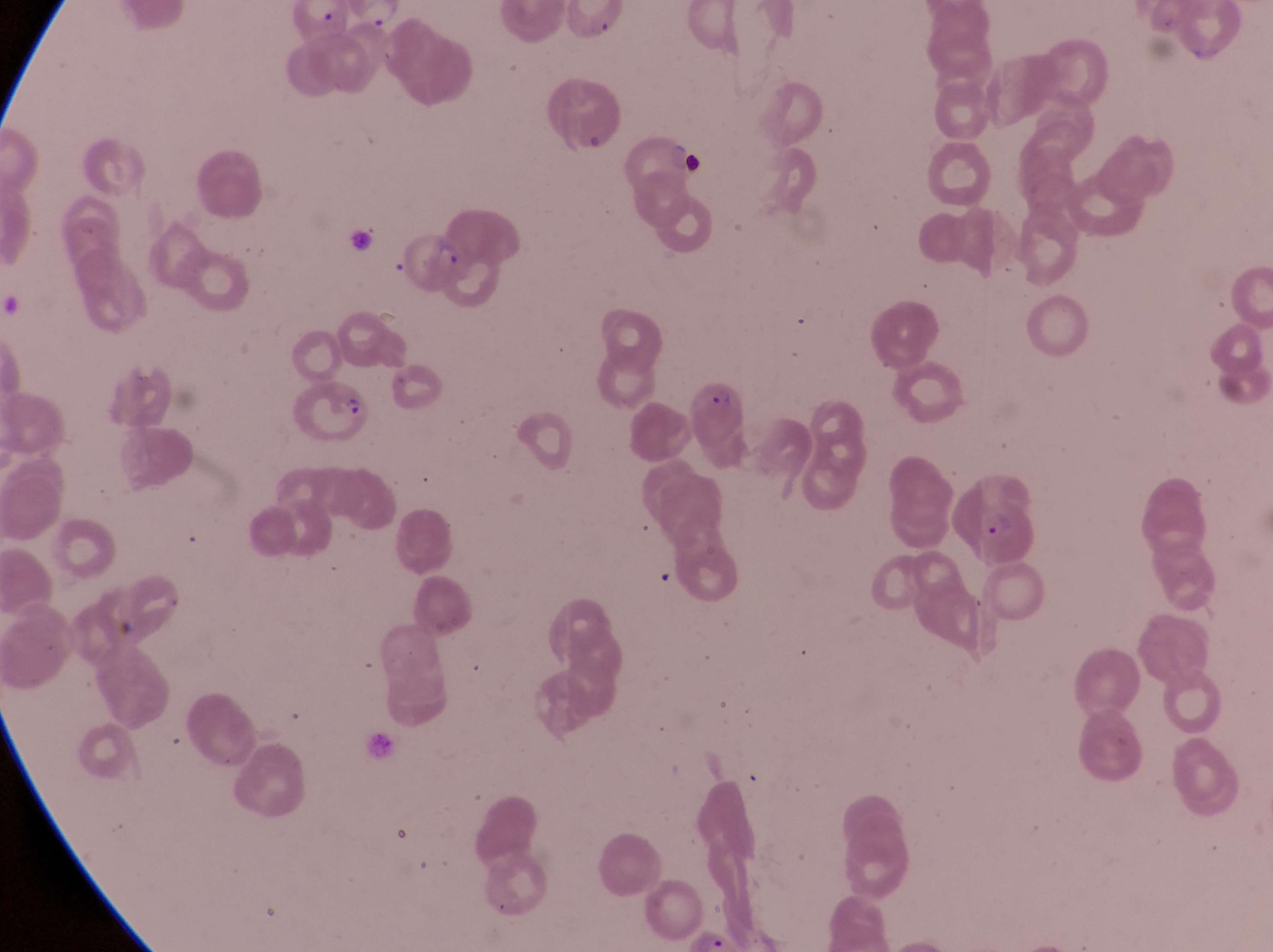
parasitised_red_blood_cell_locations: 'approximate bounding boxes as (left, top, right, bottom) in pixels: (404, 227, 469, 299), (289, 375, 374, 445), (696, 377, 751, 454), (968, 489, 1042, 567)'
preparation: thin blood smear
magnification: 1000x
image_size: 1273×952 pixels
country: Uganda
artifact_platelet_like_body_stain_precipitate_or_debris_locations: 'approximate bounding boxes as (left, top, right, bottom) in pixels: (682, 152, 707, 184)'
field_of_view: single
capture: smartphone photograph through the eyepiece of an Olympus CX-23 microscope